Classify this cell by malaria status.
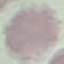

It is uninfected.

Giemsa stain. Thin blood smear. Automatically extracted cell patch, resized to 64 × 64 pixels. Acquired by smartphone through the microscope eyepiece.